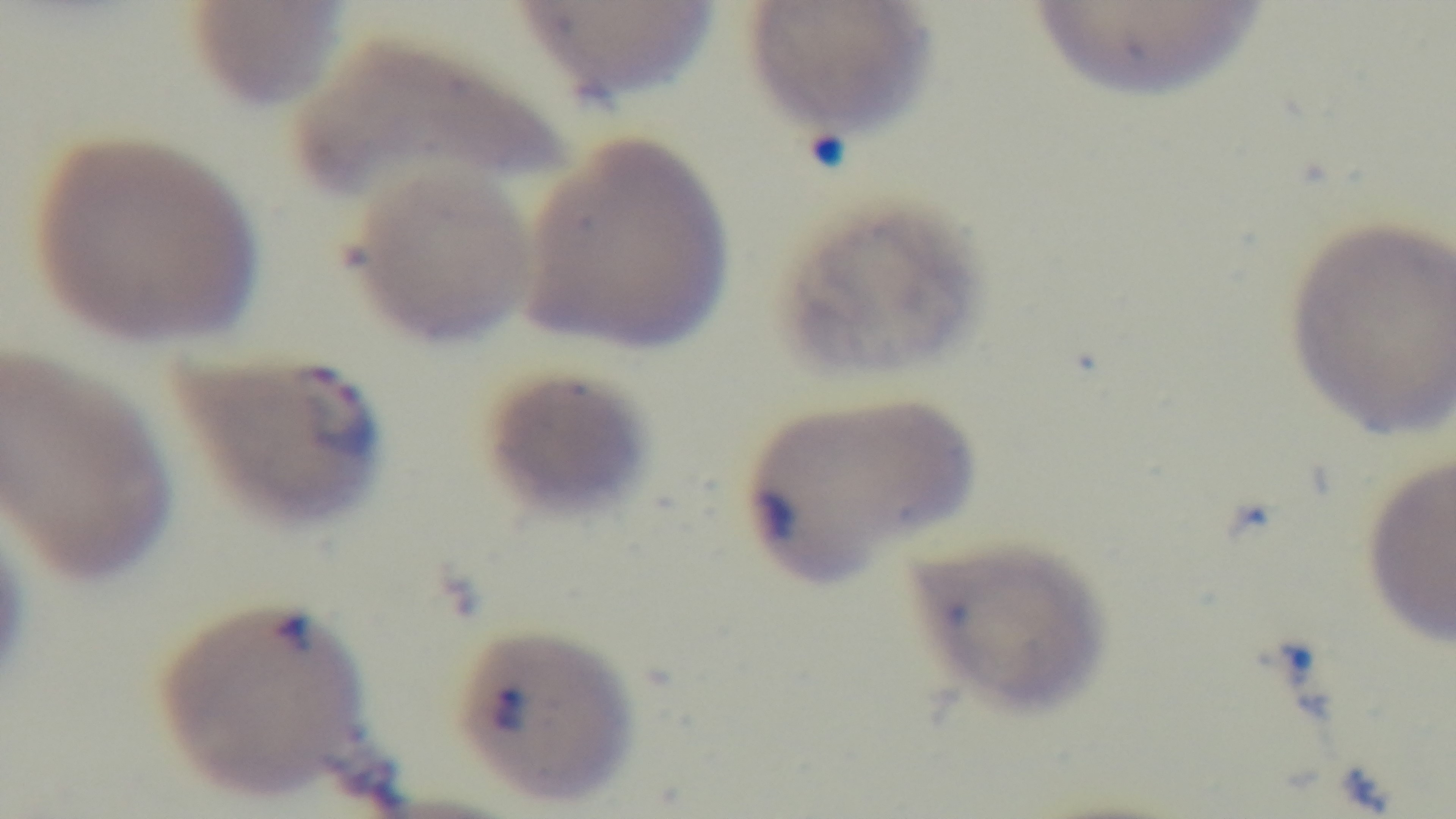
Summary:
  - Modality: light microscopy
  - Capture: mounted 4K digital camera
  - Objective: 100x oil immersion
  - Field of view: one from the slide
  - Preparation: thin smear
  - Stain: Giemsa
  - Malaria status: infected